Assess this cell for malaria.
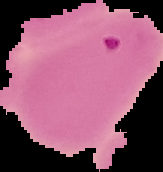
Parasitized.

Segmented cell region on a black background. Image is 163×172 pixels. From a thin blood smear.